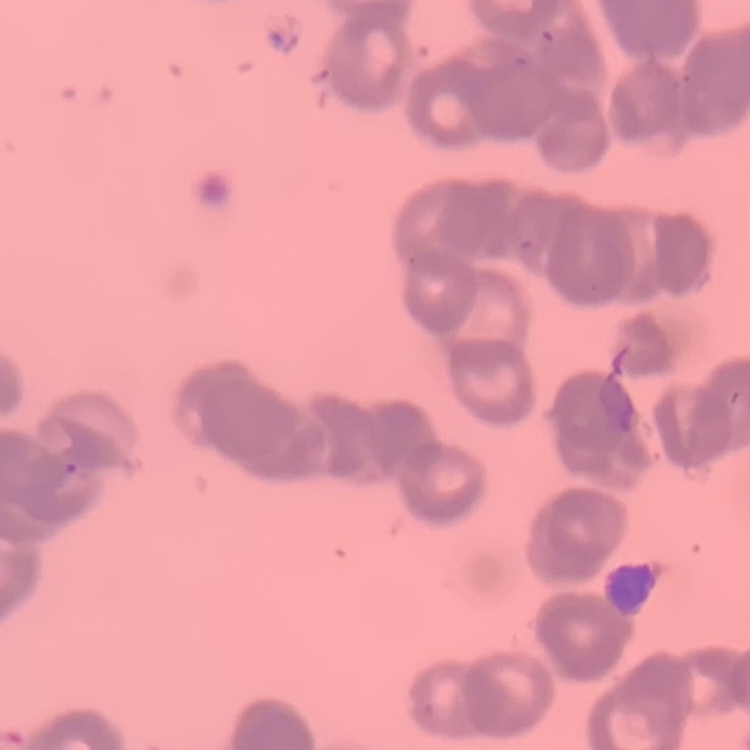
Summary:
  - Erythrocyte morphology: rouleaux formation
  - Stain: Field's or Giemsa
  - Image type: one tile cut from a larger photomicrograph
  - Preparation: thin blood smear